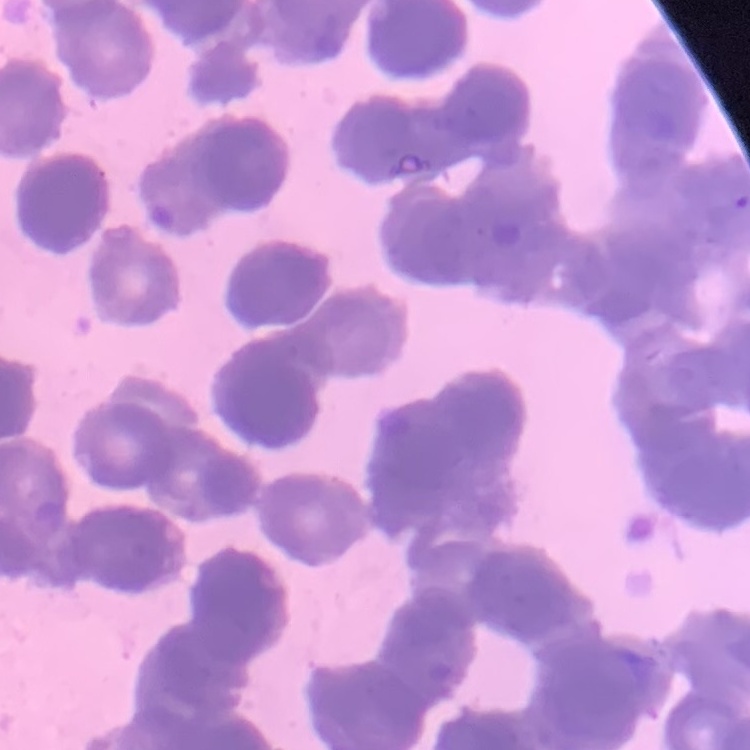

The erythrocytes show rouleaux formation. One tile cut from a larger photomicrograph. Thin peripheral smear. Stained with either Field's or Giemsa.